Give the extent of all uninfected red blood cells.
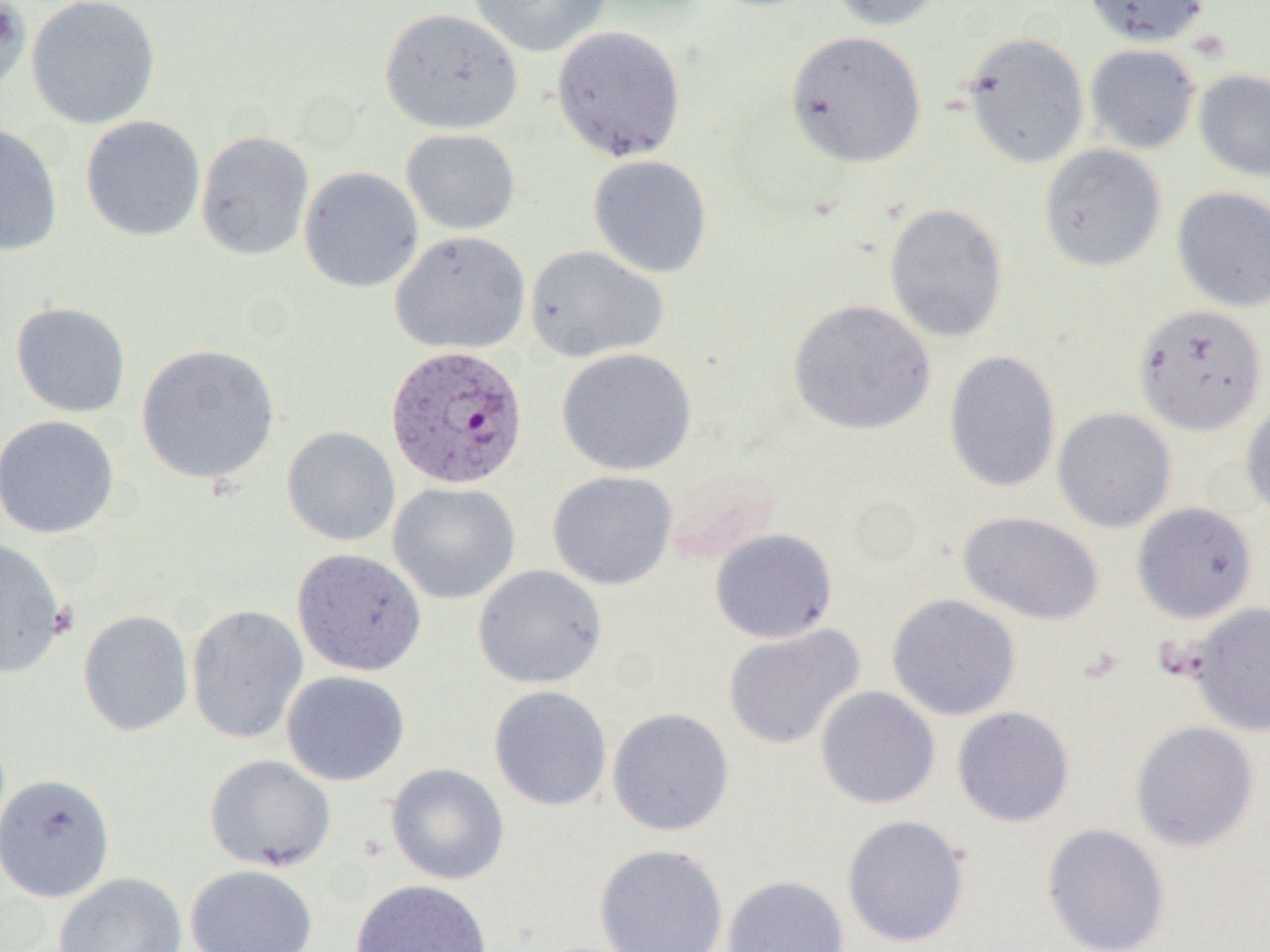
Approximate bounding boxes as (x1, y1, x2, y2) in pixels.
Uninfected red blood cells: (0, 0, 32, 99), (25, 0, 162, 130), (466, 0, 612, 58), (825, 0, 946, 32), (1082, 0, 1210, 47), (379, 7, 524, 135), (551, 24, 687, 162), (784, 30, 927, 168), (961, 31, 1090, 169), (1084, 43, 1200, 154), (1193, 68, 1270, 183), (80, 115, 206, 242), (0, 121, 64, 256), (400, 128, 521, 236), (195, 131, 315, 261), (1038, 144, 1167, 274), (588, 154, 713, 279), (298, 166, 424, 293), (1170, 186, 1270, 313), (884, 202, 1009, 343), (390, 230, 531, 355), (524, 245, 669, 364), (788, 299, 936, 436), (10, 301, 131, 418), (1134, 303, 1267, 436), (136, 344, 282, 486), (556, 347, 697, 476), (943, 350, 1061, 494), (1240, 395, 1270, 521), (1052, 407, 1176, 533), (0, 415, 120, 540), (281, 426, 401, 546), (547, 470, 678, 590), (388, 482, 521, 605), (1132, 501, 1258, 623), (958, 511, 1104, 625), (709, 527, 838, 644), (0, 538, 67, 679), (292, 549, 427, 676), (473, 564, 608, 689), (887, 593, 1021, 720), (1189, 602, 1270, 737), (186, 604, 309, 744), (77, 609, 194, 737), (722, 622, 865, 750), (281, 670, 411, 786), (488, 685, 612, 812), (814, 685, 940, 809), (951, 706, 1075, 827), (606, 707, 735, 837), (1130, 721, 1260, 852), (204, 754, 337, 872), (385, 762, 510, 885), (0, 772, 116, 903), (841, 814, 970, 948), (1041, 822, 1171, 952), (594, 843, 729, 952), (185, 863, 318, 952), (53, 871, 188, 952), (722, 874, 850, 952), (350, 879, 493, 952).

Plasmodium vivax-infected red blood cell locations: (385, 345, 530, 491). Slide-level diagnosis: Plasmodium vivax. Light microscopy. One field of a larger specimen. 1000x magnification. Thin blood smear. Image is 1270×952 pixels.